Identify the parasite.
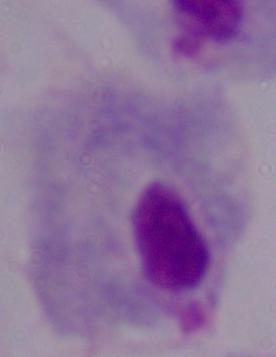
This is a trichomonad.

modality: photomicrograph
magnification: 1000x